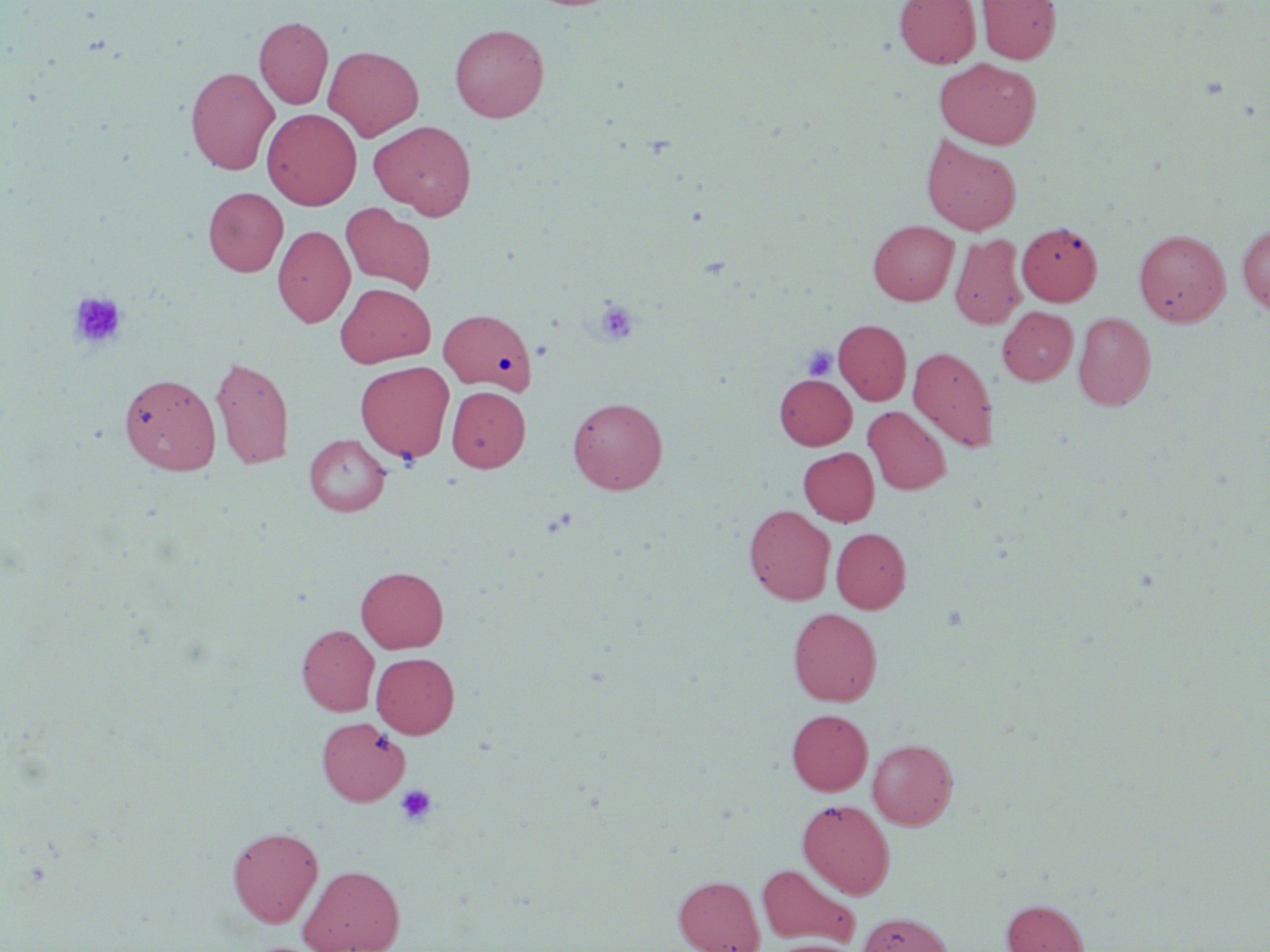 Approximate bounding boxes as [x1, y1, x2, y2] in pixels. Platelet locations: [69, 291, 128, 350], [593, 299, 640, 346], [803, 346, 837, 381], [395, 784, 437, 825]. Uninfected red blood cell locations: [894, 0, 981, 68], [977, 0, 1060, 64], [254, 16, 333, 109], [450, 24, 549, 122], [324, 45, 423, 141], [934, 58, 1041, 149], [186, 66, 279, 175], [262, 108, 362, 210], [370, 120, 477, 219], [921, 135, 1022, 235], [203, 187, 288, 276], [340, 202, 436, 294], [868, 220, 958, 305], [1017, 222, 1102, 305], [1237, 223, 1270, 314], [272, 225, 355, 328], [1134, 229, 1231, 326], [950, 234, 1027, 329], [335, 282, 435, 368], [998, 306, 1077, 385], [438, 308, 537, 393], [1073, 311, 1156, 410], [833, 319, 911, 405], [908, 346, 998, 451], [210, 356, 294, 469], [355, 361, 454, 462], [119, 373, 221, 475], [774, 374, 856, 449], [447, 386, 530, 472], [567, 396, 668, 494], [863, 406, 951, 495], [304, 434, 390, 516], [799, 447, 879, 526], [744, 505, 836, 604], [831, 527, 911, 613], [356, 566, 448, 653], [788, 607, 882, 706], [297, 625, 379, 715], [371, 652, 459, 738], [787, 708, 872, 795], [317, 716, 410, 805], [868, 738, 958, 830], [797, 798, 894, 899], [227, 825, 323, 927], [756, 863, 860, 948], [299, 864, 406, 952], [674, 874, 764, 952], [1001, 899, 1088, 952], [858, 911, 954, 952], [764, 939, 860, 952]. Slide-level diagnosis: no evidence of blood parasites. One field of a larger specimen. Image is 1270×952 pixels. Light microscopy. Thin blood film. May-Grünwald-Giemsa-stained preparation. 1000x magnification.